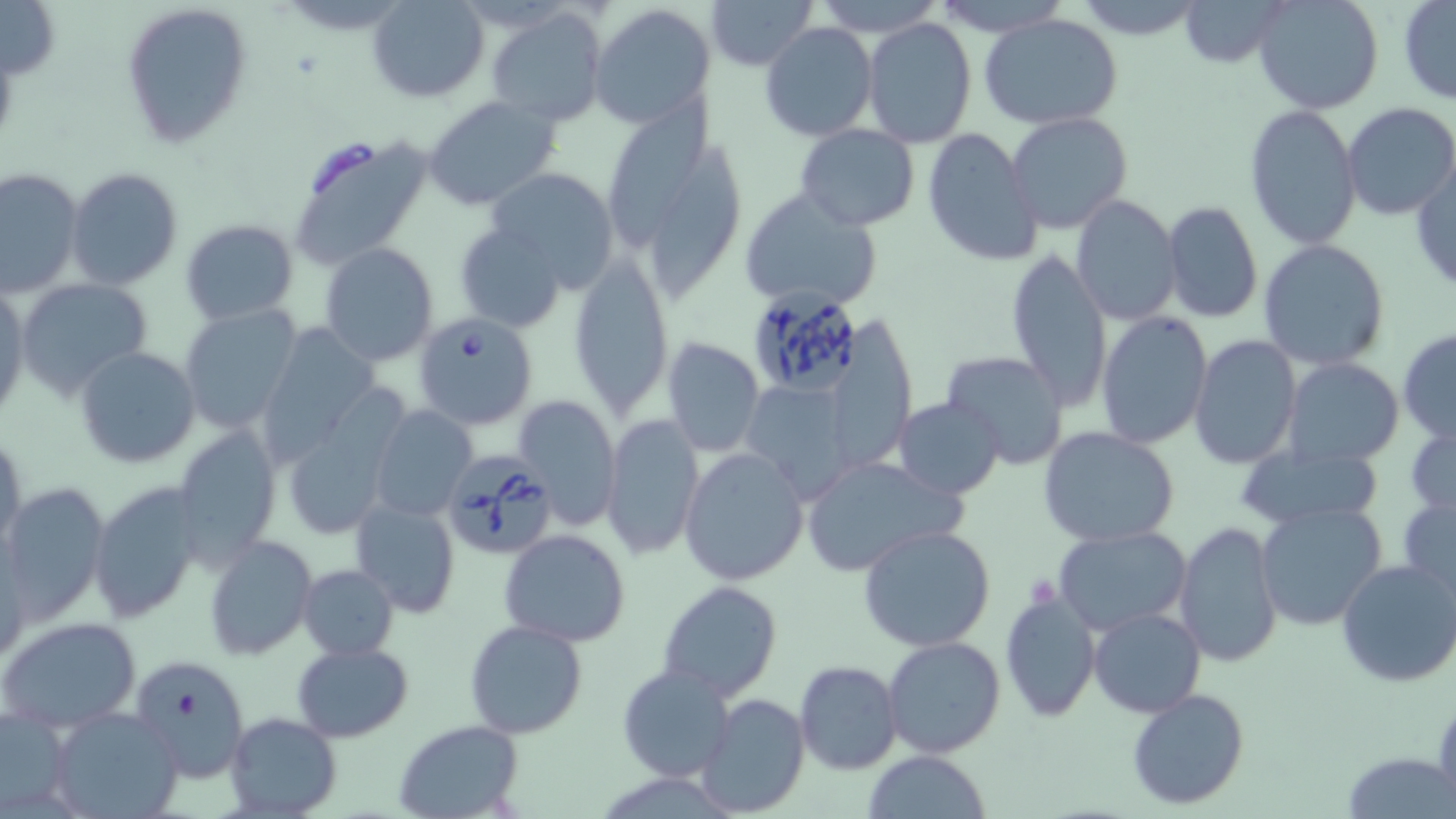
slide-level diagnosis = Babesia divergens
magnification = 1000x
Babesia divergens-infected red blood cell locations = approximate bounding boxes as [x1, y1, x2, y2] in pixels: [745, 291, 868, 398], [416, 312, 538, 429], [438, 450, 556, 562]
field of view = single
stain = May-Grünwald-Giemsa
uninfected red blood cell locations = approximate bounding boxes as [x1, y1, x2, y2] in pixels: [367, 0, 489, 104], [704, 0, 818, 69], [813, 0, 947, 37], [930, 0, 1074, 36], [1072, 0, 1208, 39], [1179, 0, 1290, 67], [1253, 0, 1384, 116], [0, 1, 60, 79], [1397, 1, 1456, 105], [122, 2, 254, 147], [588, 4, 717, 129], [488, 6, 607, 126], [980, 15, 1124, 129], [862, 17, 977, 149], [759, 21, 878, 141], [612, 88, 715, 258], [423, 94, 562, 210], [1244, 104, 1363, 251], [1341, 104, 1456, 221], [1005, 111, 1133, 235], [796, 124, 920, 231], [922, 129, 1041, 268], [285, 134, 431, 270], [649, 146, 746, 304], [1411, 158, 1456, 296], [485, 165, 622, 290], [66, 167, 184, 290], [0, 168, 83, 297], [738, 188, 883, 311], [1069, 194, 1182, 325], [1161, 200, 1263, 323], [181, 219, 300, 326], [454, 223, 566, 332], [1258, 238, 1390, 371], [320, 242, 439, 367], [1006, 248, 1112, 413], [570, 252, 673, 416], [15, 276, 154, 400], [0, 286, 29, 420], [179, 305, 303, 433], [1096, 311, 1213, 450], [256, 323, 379, 466], [1398, 328, 1455, 443], [1189, 334, 1302, 469], [660, 336, 765, 457], [75, 346, 201, 469], [940, 351, 1070, 469], [1283, 358, 1405, 469], [741, 377, 856, 500], [514, 396, 621, 531], [893, 397, 1005, 499], [371, 405, 478, 523], [1406, 410, 1456, 521], [600, 413, 706, 562], [850, 416, 998, 553], [1038, 425, 1180, 547], [173, 426, 282, 563], [1, 429, 26, 557], [1231, 443, 1386, 530], [679, 447, 810, 586], [799, 454, 966, 577], [91, 480, 203, 621], [1, 481, 110, 625], [1398, 494, 1456, 607], [351, 497, 460, 620], [1256, 502, 1388, 630], [1175, 522, 1283, 669], [859, 524, 998, 651], [1053, 526, 1192, 637], [500, 529, 630, 646], [205, 535, 317, 659], [1, 540, 31, 668], [1335, 559, 1456, 687], [298, 563, 398, 659], [658, 580, 783, 700], [1000, 591, 1101, 722], [1088, 608, 1206, 718], [0, 615, 142, 732], [464, 618, 590, 740], [880, 637, 1005, 758], [291, 642, 413, 742], [129, 653, 251, 781], [794, 660, 902, 773], [617, 665, 737, 782], [1126, 687, 1252, 810], [695, 692, 811, 816], [47, 706, 183, 819], [1, 708, 74, 816], [224, 711, 342, 818], [393, 719, 523, 819], [1344, 749, 1451, 818], [864, 750, 992, 819]
image size = 1456×819 pixels
modality = light microscopy
preparation = thin blood smear